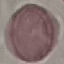
Result: negative for malaria parasites. Giemsa stain. Automatically extracted cell patch, resized to 64 × 64 pixels. Thin blood film. Acquired by smartphone through the microscope eyepiece.